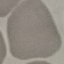

Summary:
  - Result: no malaria parasites seen
  - Stain: Giemsa
  - Image type: automatically extracted cell patch, resized to 64 × 64 pixels
  - Capture: smartphone camera at the microscope eyepiece
  - Preparation: thin smear